State the blood parasite species.
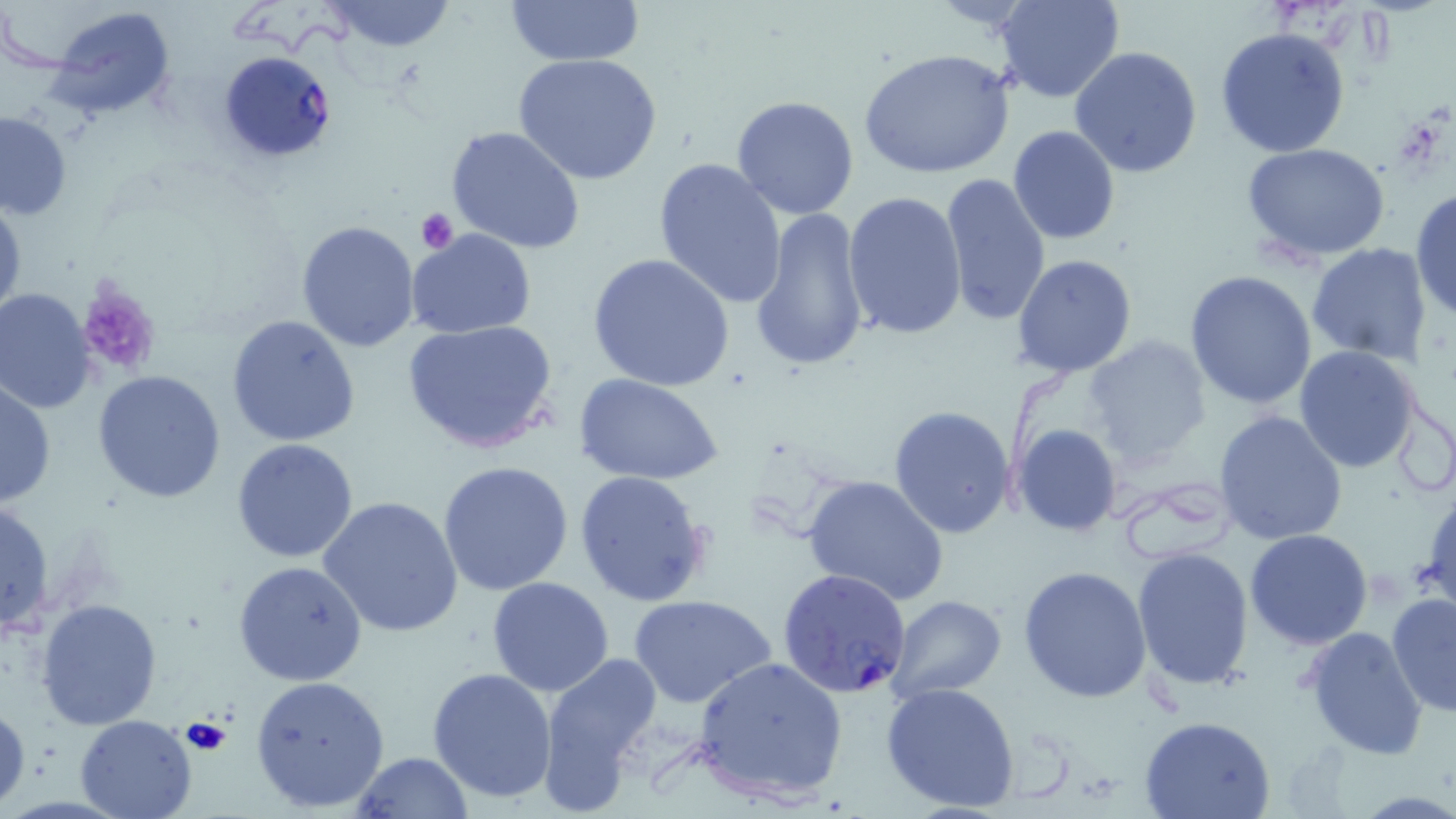
Plasmodium falciparum.

Summary:
  - Coordinate format: approximate bounding boxes as (x1,y1)-(x2,y2) corner pairs in pixels
  - Uninfected red blood cell locations: (327,0)-(458,52), (503,0)-(645,68), (994,0)-(1125,104), (46,4)-(178,122), (1214,26)-(1351,159), (1069,46)-(1205,178), (861,48)-(1014,180), (514,52)-(664,186), (730,96)-(860,221), (0,110)-(73,221), (444,124)-(587,255), (1008,126)-(1121,244), (1244,143)-(1390,262), (652,156)-(788,307), (939,171)-(1052,328), (1409,187)-(1456,322), (0,191)-(26,328), (843,192)-(967,342), (748,205)-(872,374), (296,221)-(421,353), (406,230)-(537,339), (1304,243)-(1434,367), (1012,253)-(1137,378), (588,254)-(735,393), (1185,271)-(1318,410), (1,288)-(98,413), (227,313)-(362,448), (402,319)-(559,453), (1083,335)-(1211,467), (1293,345)-(1423,474), (93,369)-(225,505), (574,374)-(723,488), (0,377)-(55,509), (888,405)-(1019,541), (1214,410)-(1348,545), (1011,423)-(1122,536), (231,438)-(361,562), (437,460)-(574,597), (575,469)-(713,606), (803,475)-(950,605), (1420,482)-(1456,618), (318,495)-(463,637), (1,499)-(53,638), (1243,528)-(1373,650), (1132,545)-(1254,690), (232,560)-(367,685), (1018,565)-(1152,703), (487,577)-(615,696), (1386,591)-(1456,718), (628,593)-(777,710), (885,594)-(1008,702), (36,597)-(163,730), (1302,625)-(1430,760), (536,649)-(663,810), (693,655)-(849,805), (427,667)-(558,803), (248,673)-(389,814), (881,681)-(1023,814), (0,700)-(29,812), (75,714)-(198,819), (1140,714)-(1276,818), (350,752)-(475,818)
  - Platelet locations: (416,209)-(459,253), (77,284)-(161,377), (180,715)-(230,758)
  - Plasmodium falciparum-infected red blood cell locations: (217,52)-(338,163), (777,567)-(914,697)
  - Field of view: single
  - Magnification: 1000x
  - Preparation: thin blood film
  - Image size: 1456×819 pixels
  - Modality: light microscopy
  - Stain: May-Grünwald-Giemsa